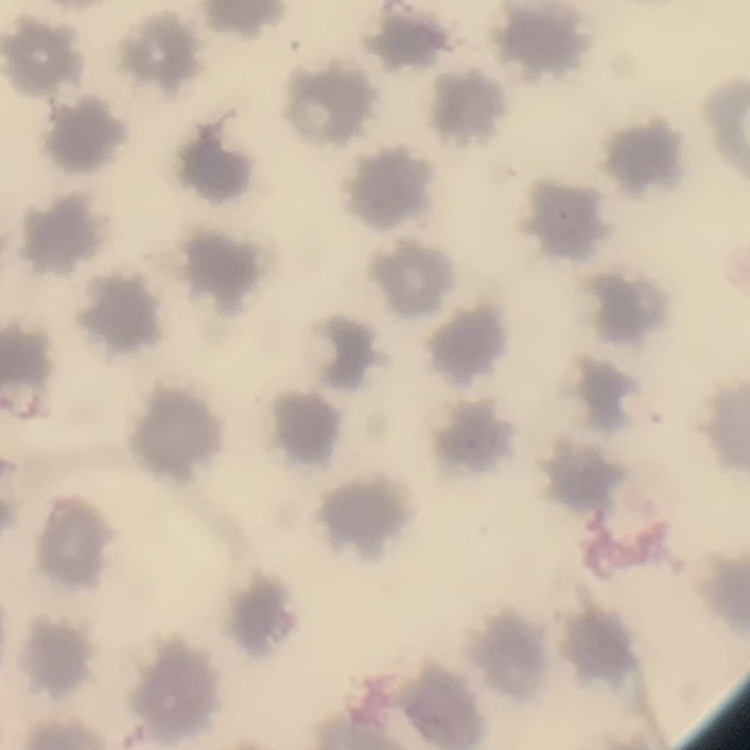

Summary:
  - Red blood cell morphology: no rouleaux formation
  - Image type: square crop of a larger photomicrograph
  - Stain: Field's or Giemsa
  - Preparation: thin blood film